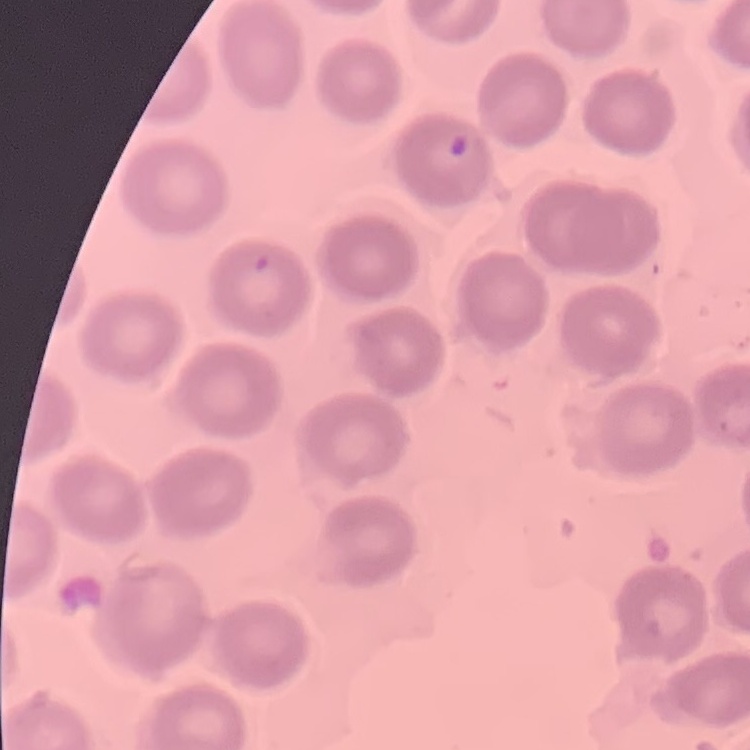

red blood cell morphology = no rouleaux formation
stain = Field's or Giemsa
preparation = thin peripheral smear
image type = one tile cut from a larger photomicrograph